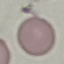

Summary:
  - Result: no malaria parasites detected
  - Stain: Giemsa
  - Image type: automatically extracted cell patch, resized to 64 × 64 pixels
  - Capture: smartphone through the microscope eyepiece
  - Preparation: thin blood smear